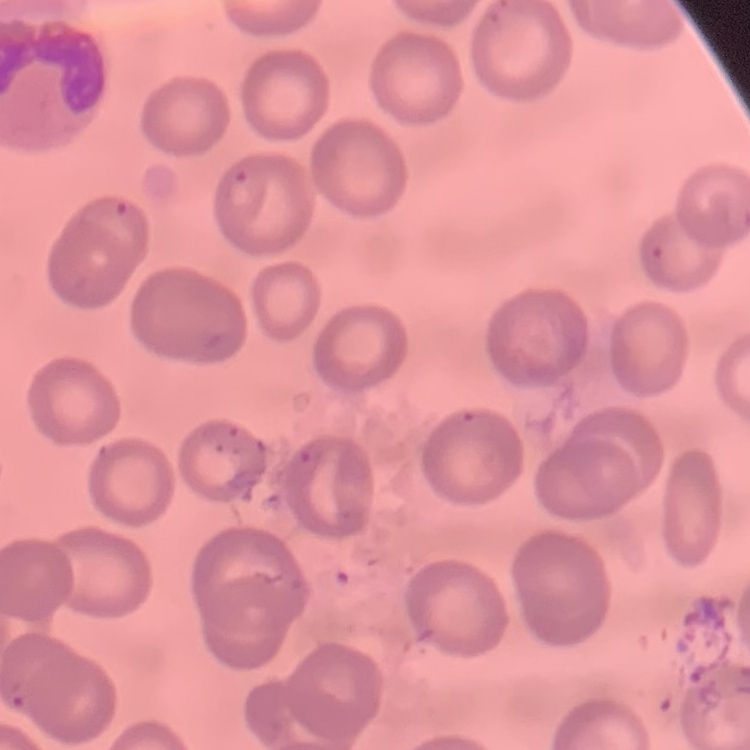

The red blood cells show no rouleaux formation. Thin blood film. One tile cut from a larger photomicrograph. Stained with either Field's or Giemsa.